Outline each blood parasite and name the species.
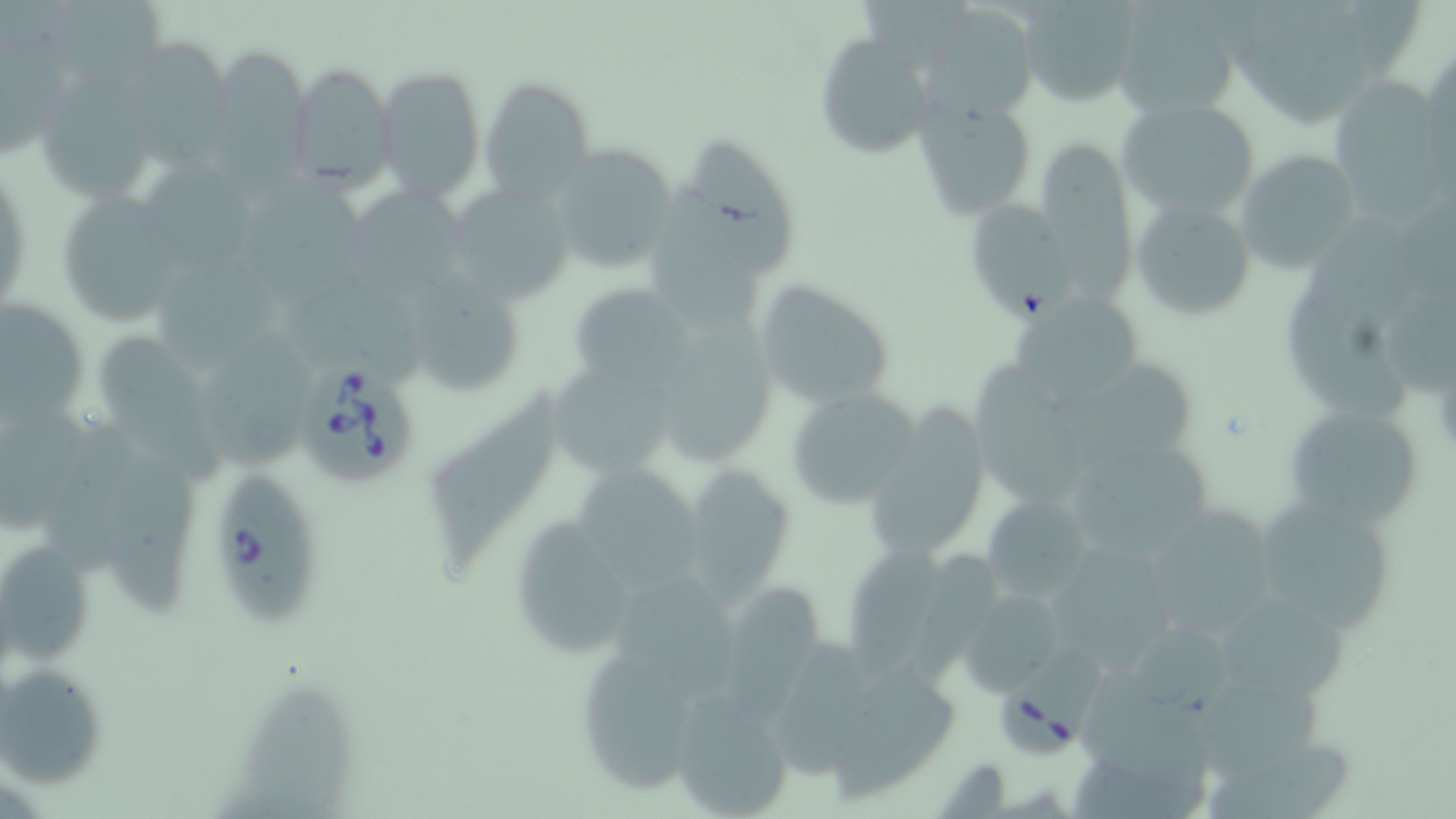

Approximate bounding boxes as named x1/y1/x2/y2 corners in pixels.
Babesia divergens-infected red blood cells: (x1=299, y1=363, x2=418, y2=485), (x1=214, y1=474, x2=318, y2=629), (x1=997, y1=682, x2=1089, y2=756).
No Plasmodium falciparum, Plasmodium ovale, Plasmodium malariae, Plasmodium vivax, or Trypanosoma brucei observed.

slide-level diagnosis = Babesia divergens
modality = light microscopy
uninfected red blood cell locations = approximate bounding boxes as named x1/y1/x2/y2 corners in pixels: (x1=42, y1=0, x2=163, y2=91), (x1=1014, y1=0, x2=1142, y2=105), (x1=1110, y1=0, x2=1243, y2=119), (x1=922, y1=10, x2=1042, y2=117), (x1=0, y1=16, x2=73, y2=157), (x1=810, y1=33, x2=931, y2=161), (x1=118, y1=40, x2=231, y2=175), (x1=1421, y1=47, x2=1455, y2=172), (x1=208, y1=48, x2=315, y2=208), (x1=289, y1=62, x2=394, y2=192), (x1=375, y1=65, x2=486, y2=200), (x1=478, y1=75, x2=595, y2=200), (x1=1328, y1=75, x2=1449, y2=210), (x1=41, y1=80, x2=147, y2=205), (x1=1117, y1=98, x2=1262, y2=224), (x1=915, y1=100, x2=1037, y2=222), (x1=688, y1=138, x2=800, y2=278), (x1=1038, y1=139, x2=1137, y2=315), (x1=546, y1=144, x2=677, y2=274), (x1=1233, y1=150, x2=1362, y2=272), (x1=145, y1=161, x2=252, y2=274), (x1=246, y1=179, x2=372, y2=315), (x1=349, y1=183, x2=472, y2=298), (x1=649, y1=183, x2=766, y2=335), (x1=460, y1=189, x2=568, y2=301), (x1=63, y1=194, x2=180, y2=328), (x1=1130, y1=197, x2=1257, y2=320), (x1=970, y1=200, x2=1078, y2=330), (x1=154, y1=260, x2=275, y2=378), (x1=415, y1=269, x2=516, y2=391), (x1=288, y1=274, x2=426, y2=389), (x1=1284, y1=275, x2=1409, y2=424), (x1=753, y1=279, x2=897, y2=414), (x1=568, y1=281, x2=693, y2=392), (x1=1389, y1=287, x2=1455, y2=400), (x1=1018, y1=292, x2=1145, y2=405), (x1=0, y1=306, x2=82, y2=427), (x1=667, y1=317, x2=772, y2=464), (x1=206, y1=329, x2=320, y2=474), (x1=97, y1=337, x2=222, y2=487), (x1=549, y1=360, x2=674, y2=477), (x1=1051, y1=362, x2=1200, y2=471), (x1=974, y1=364, x2=1093, y2=505), (x1=784, y1=384, x2=923, y2=511), (x1=428, y1=390, x2=558, y2=578), (x1=1282, y1=402, x2=1428, y2=529), (x1=0, y1=404, x2=89, y2=533), (x1=867, y1=404, x2=982, y2=554), (x1=48, y1=417, x2=143, y2=581), (x1=1071, y1=452, x2=1210, y2=554), (x1=103, y1=454, x2=200, y2=616), (x1=576, y1=468, x2=704, y2=590), (x1=691, y1=470, x2=791, y2=608), (x1=1249, y1=491, x2=1403, y2=636), (x1=981, y1=492, x2=1094, y2=597), (x1=1154, y1=508, x2=1271, y2=636), (x1=522, y1=515, x2=632, y2=654), (x1=846, y1=543, x2=946, y2=689), (x1=0, y1=548, x2=94, y2=663), (x1=1058, y1=549, x2=1176, y2=673), (x1=612, y1=578, x2=740, y2=703), (x1=724, y1=582, x2=821, y2=723), (x1=958, y1=587, x2=1067, y2=696), (x1=1221, y1=599, x2=1349, y2=707), (x1=773, y1=632, x2=873, y2=784), (x1=579, y1=652, x2=695, y2=793), (x1=1, y1=661, x2=109, y2=788), (x1=831, y1=665, x2=961, y2=807), (x1=1076, y1=672, x2=1219, y2=795), (x1=242, y1=681, x2=356, y2=819), (x1=1202, y1=691, x2=1318, y2=777), (x1=670, y1=692, x2=795, y2=818), (x1=1205, y1=740, x2=1353, y2=817)
stain = May-Grünwald-Giemsa
preparation = thin blood smear
field of view = single
image size = 1456×819 pixels
magnification = 1000x